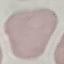

malaria_status: uninfected
capture: smartphone through the microscope eyepiece
image_type: automatically extracted cell patch, resized to 64 × 64 pixels
preparation: thin blood film
stain: Giemsa